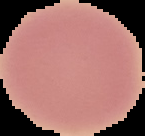

From a thin blood film. Cell region segmented out of the field of view; the surrounding area is masked to black. Image is 145×136 pixels. Malaria status: uninfected.